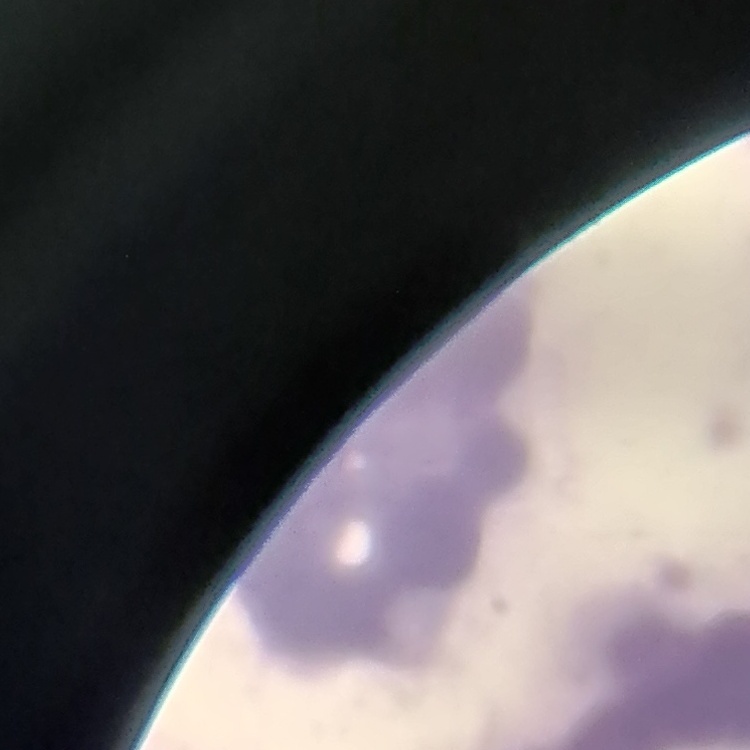
Summary:
  - Red blood cell morphology: rouleaux formation
  - Image type: one tile cut from a larger photomicrograph
  - Preparation: thin blood smear
  - Stain: Field's or Giemsa